Outline each Plasmodium vivax-infected red blood cell.
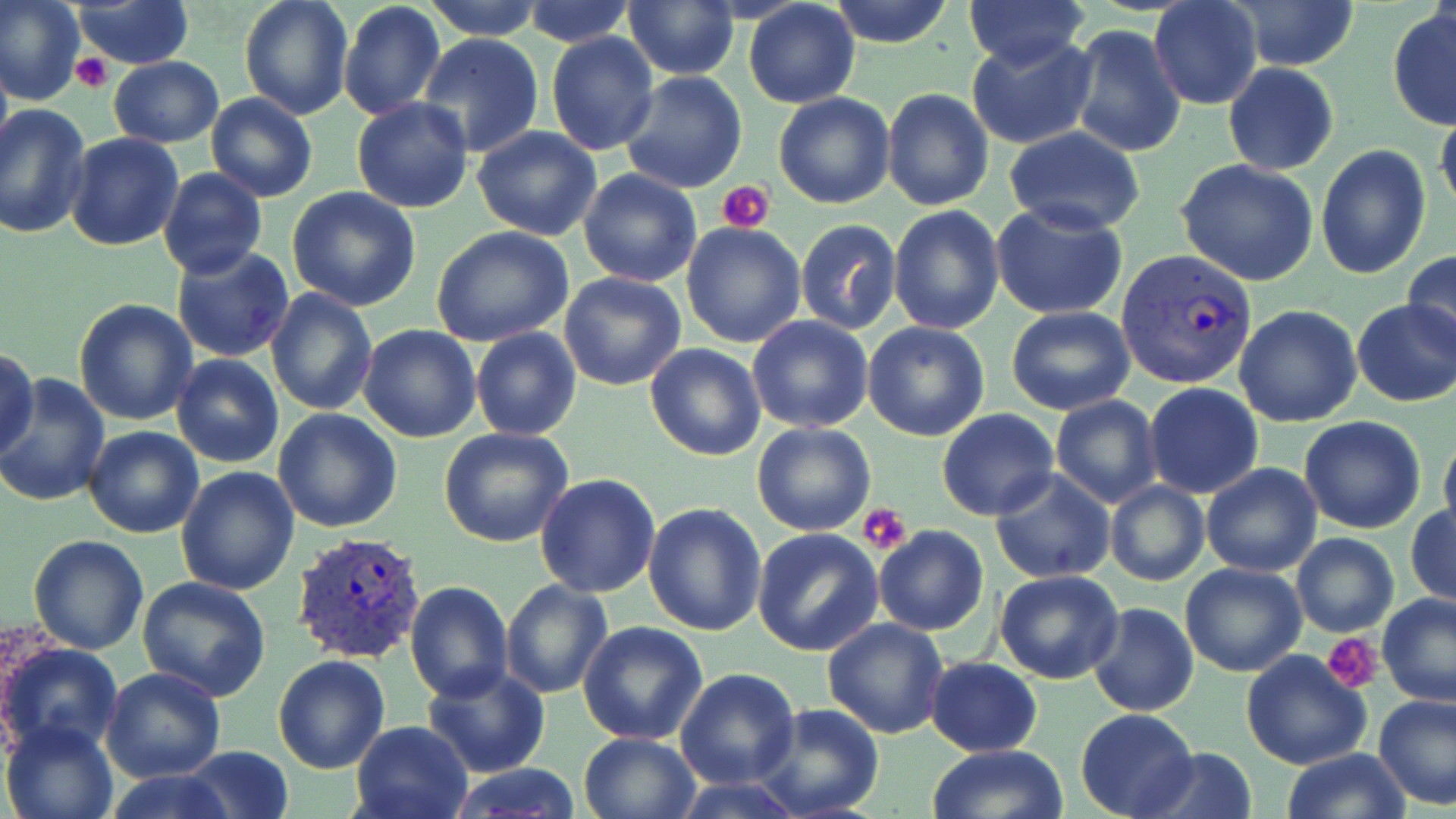

Approximate bounding boxes as (x1, y1, x2, y2) in pixels.
Plasmodium vivax-infected red blood cells: (1116, 250, 1258, 390), (290, 531, 426, 667).

Uninfected red blood cell locations: (1, 0, 85, 104), (239, 0, 355, 121), (423, 0, 545, 41), (828, 0, 955, 48), (962, 0, 1089, 69), (74, 1, 194, 69), (338, 1, 446, 119), (521, 1, 633, 47), (743, 1, 860, 110), (1233, 1, 1358, 71), (622, 2, 739, 80), (1149, 2, 1261, 111), (1387, 8, 1456, 130), (1067, 25, 1186, 158), (545, 32, 660, 156), (966, 33, 1099, 151), (417, 34, 546, 158), (0, 42, 12, 166), (107, 57, 223, 148), (1223, 62, 1338, 175), (620, 71, 748, 193), (881, 88, 993, 211), (772, 92, 894, 210), (205, 93, 318, 203), (351, 97, 473, 215), (0, 103, 92, 241), (1434, 112, 1456, 223), (472, 125, 602, 240), (1003, 126, 1147, 235), (65, 132, 184, 252), (1316, 143, 1431, 281), (1176, 158, 1319, 285), (157, 166, 266, 279), (578, 168, 702, 287), (287, 188, 422, 312), (990, 200, 1129, 321), (888, 204, 1004, 335), (794, 218, 902, 335), (681, 222, 806, 349), (432, 227, 575, 348), (170, 245, 295, 362), (1402, 250, 1456, 355), (559, 271, 688, 392), (266, 288, 377, 414), (73, 299, 197, 427), (1352, 299, 1456, 407), (1234, 305, 1364, 427), (1006, 306, 1135, 416), (747, 315, 874, 434), (862, 321, 990, 441), (358, 325, 482, 442), (470, 328, 582, 441), (644, 343, 766, 461), (1, 345, 40, 462), (170, 355, 285, 469), (0, 372, 111, 507), (1143, 382, 1264, 499), (1049, 395, 1162, 508), (273, 408, 403, 532), (937, 408, 1059, 520), (1298, 416, 1426, 535), (751, 422, 875, 536), (1439, 424, 1456, 548), (82, 425, 204, 539), (439, 428, 573, 549), (1201, 462, 1322, 577), (176, 465, 302, 595), (988, 468, 1116, 584), (535, 472, 661, 598), (1106, 480, 1209, 586), (643, 502, 767, 635), (1406, 505, 1455, 606), (874, 526, 989, 636), (751, 528, 884, 655), (1290, 532, 1399, 638), (29, 535, 149, 655), (1180, 563, 1307, 678), (994, 569, 1123, 684), (138, 576, 272, 700), (500, 578, 612, 698), (404, 581, 514, 703), (1377, 593, 1456, 707), (1087, 602, 1198, 717), (821, 616, 949, 739), (577, 621, 710, 745), (1, 640, 123, 759), (1240, 651, 1372, 770), (274, 656, 390, 774), (924, 656, 1043, 756), (421, 665, 551, 779), (101, 668, 225, 783), (675, 669, 800, 789), (1373, 691, 1456, 811), (751, 702, 884, 819), (1076, 706, 1198, 818), (0, 718, 118, 819), (348, 719, 475, 819), (578, 731, 699, 818), (928, 744, 1066, 819), (180, 746, 294, 819), (1132, 747, 1258, 819), (1280, 748, 1413, 819), (444, 763, 584, 819), (98, 769, 238, 819). Platelet locations: (72, 53, 112, 93), (718, 179, 777, 233), (860, 504, 912, 556), (1321, 633, 1383, 691). Slide-level diagnosis: Plasmodium vivax. Thin blood film. Single field of view. Captured at 1000x magnification. Optical microscopy. May-Grünwald-Giemsa-stained preparation. Image is 1456×819 pixels.